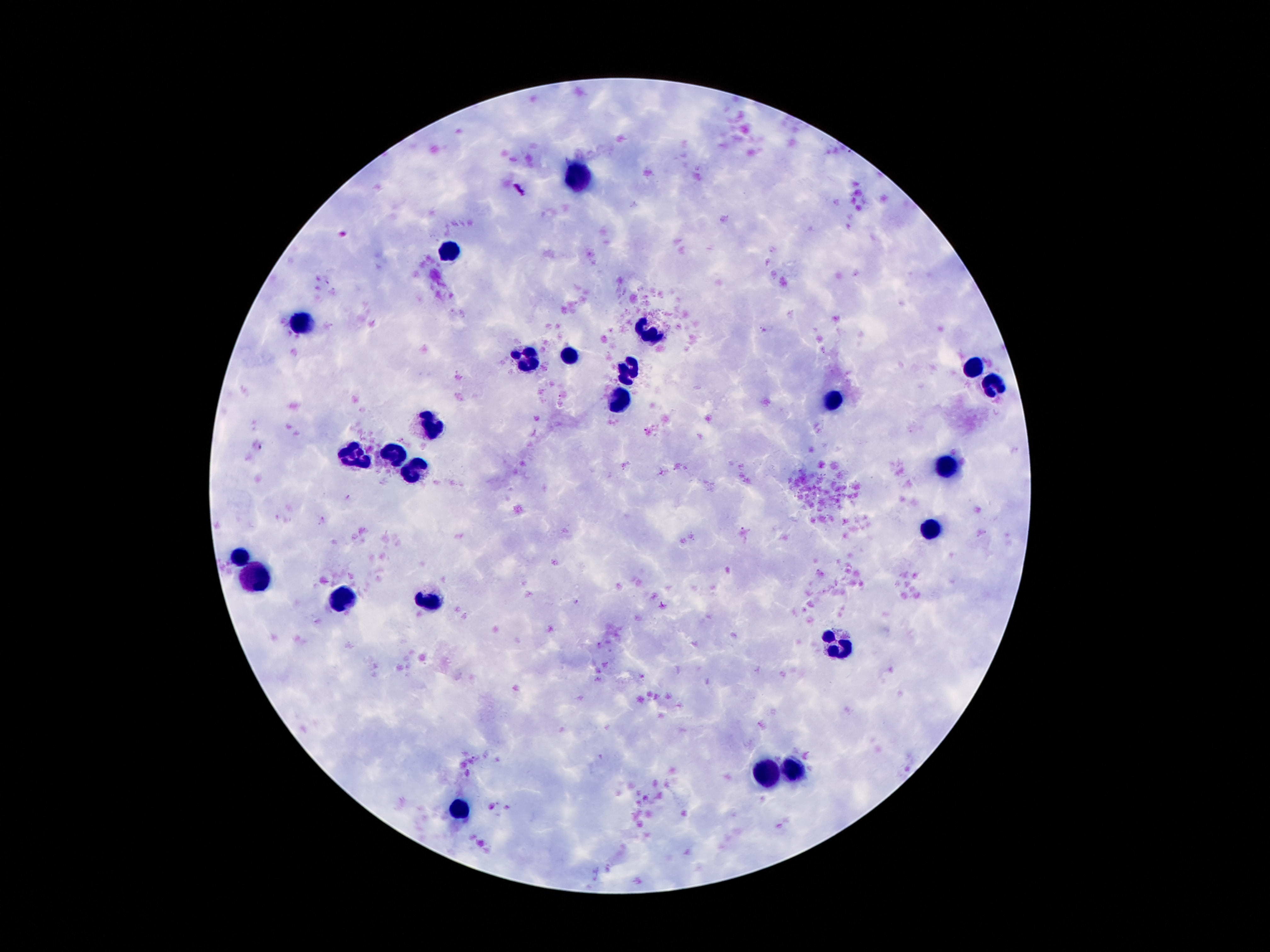

stain = Giemsa
leukocyte locations = approximate object centers, in pixels from the top-left corner: (x=578, y=178), (x=451, y=249), (x=304, y=325), (x=651, y=332), (x=526, y=356), (x=570, y=357), (x=974, y=369), (x=629, y=371), (x=992, y=385), (x=620, y=399), (x=831, y=399), (x=429, y=422), (x=397, y=453), (x=354, y=454), (x=946, y=465), (x=415, y=474), (x=932, y=530), (x=594, y=553), (x=240, y=558), (x=256, y=577), (x=424, y=601), (x=340, y=602), (x=835, y=644), (x=792, y=770), (x=767, y=776), (x=456, y=811)
field of view = single
image size = 1270×952 pixels
capture = smartphone camera through the microscope eyepiece
magnification = 100x
patient malaria status = uninfected
preparation = thick blood smear